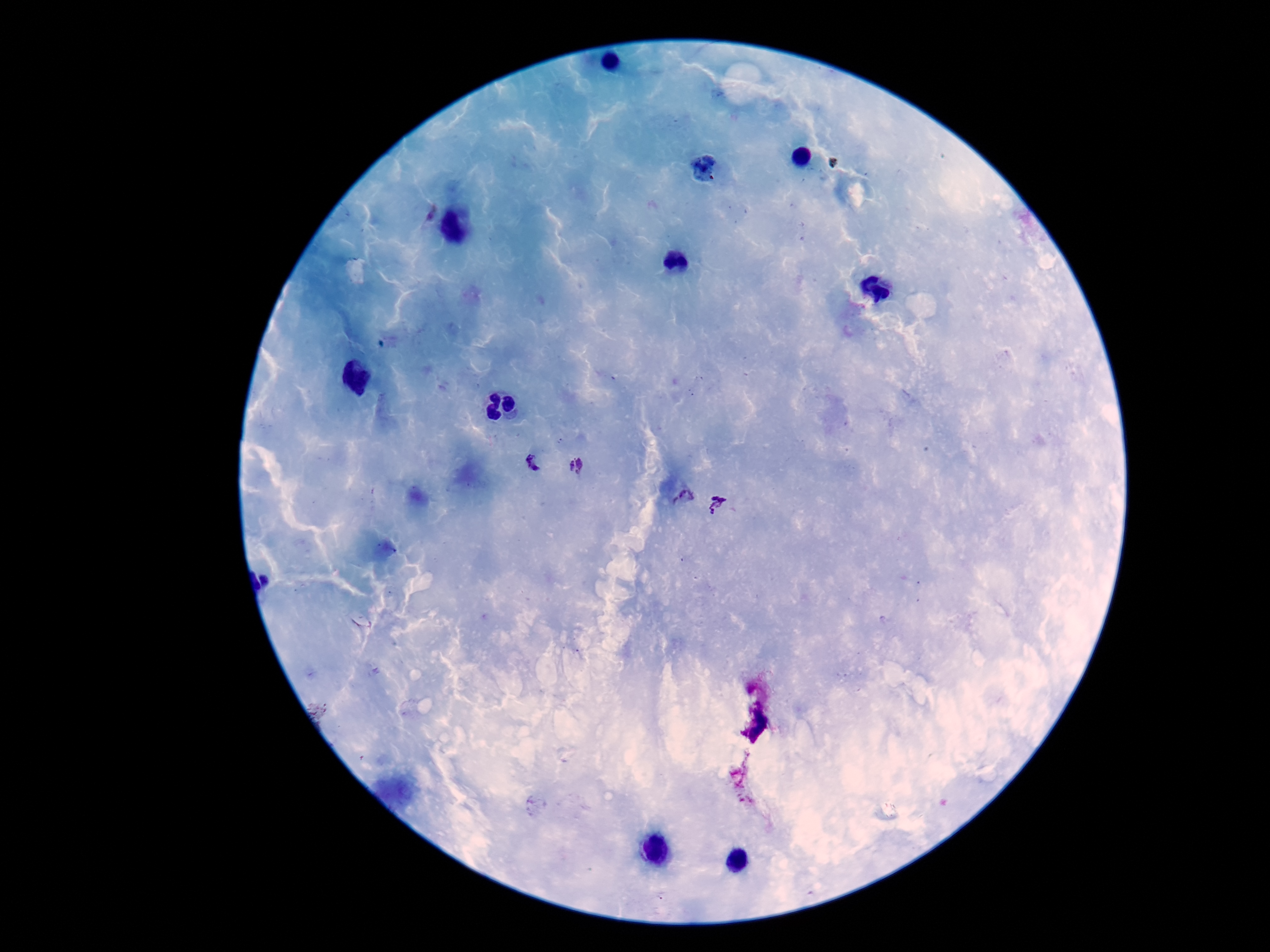

Approximate centers as {x, y} in pixels. Plasmodium parasite locations: {533, 462}, {575, 467}, {684, 498}, {716, 506}. Patient malaria status: positive. 100x magnification. Thick blood film. Image is 1270×952 pixels. Giemsa stain. Single field of view. Photographed through the microscope eyepiece with a smartphone camera.